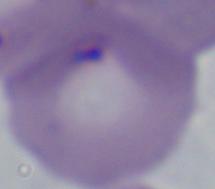

identification: Babesia
modality: photomicrograph
magnification: 1000x